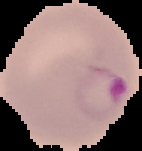
image size = 142×151 pixels
image type = segmented cell region on a black background
preparation = thin blood film
result = Plasmodium parasites identified